Locate every blood parasite and identify its species.
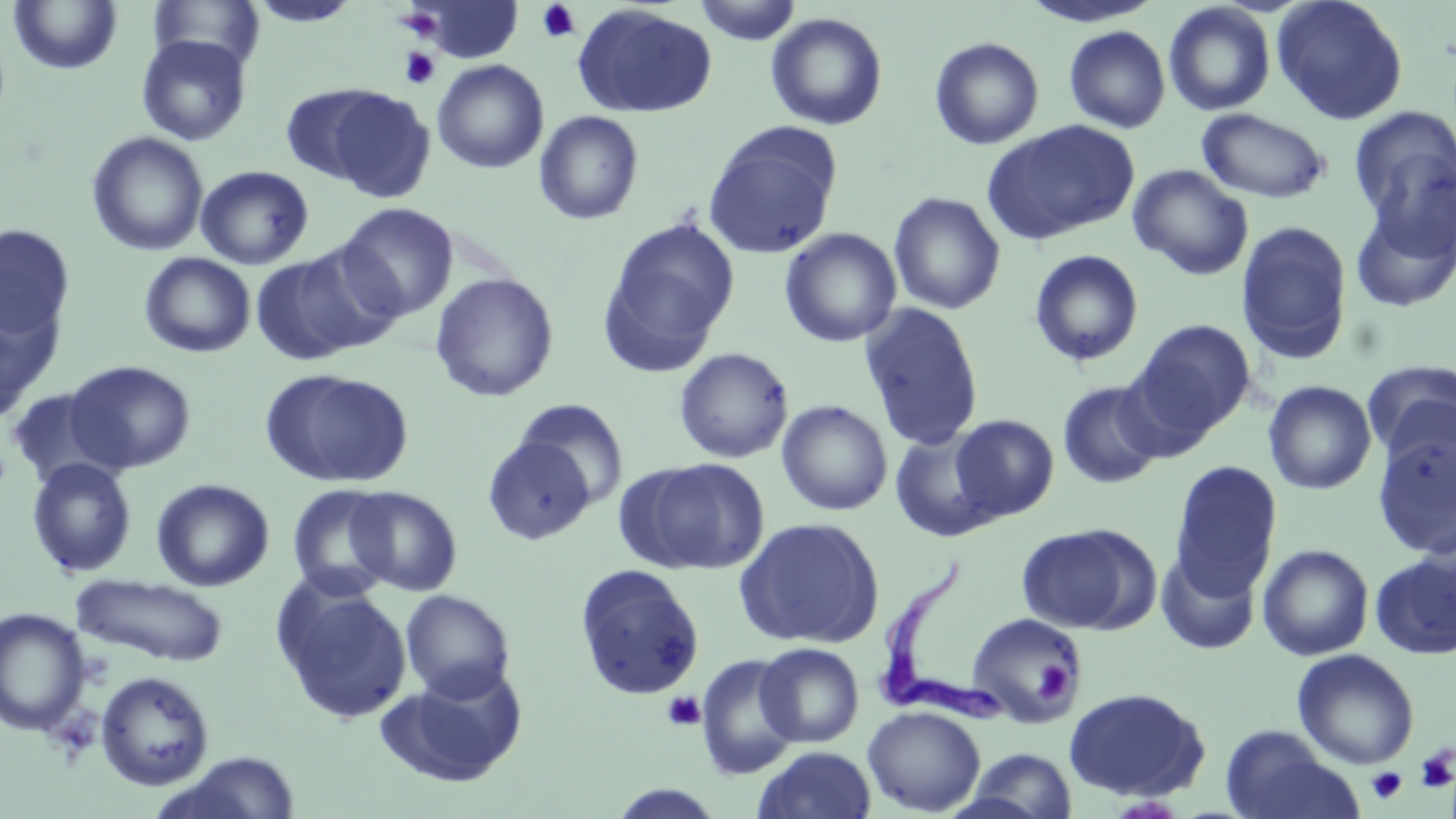
Approximate bounding boxes as named x1/y1/x2/y2 corners in pixels.
Trypanosoma brucei: (x1=876, y1=556, x2=1001, y2=721).
No Plasmodium falciparum, Plasmodium ovale, Plasmodium malariae, Plasmodium vivax, or Babesia divergens observed.

slide-level diagnosis = Trypanosoma brucei
image size = 1456×819 pixels
uninfected red blood cell locations = approximate bounding boxes as named x1/y1/x2/y2 corners in pixels: (x1=7, y1=0, x2=122, y2=76), (x1=149, y1=0, x2=265, y2=70), (x1=247, y1=0, x2=362, y2=28), (x1=692, y1=0, x2=803, y2=45), (x1=1019, y1=0, x2=1166, y2=29), (x1=1271, y1=0, x2=1409, y2=125), (x1=415, y1=1, x2=524, y2=63), (x1=1163, y1=2, x2=1276, y2=116), (x1=571, y1=5, x2=718, y2=119), (x1=399, y1=10, x2=442, y2=40), (x1=765, y1=12, x2=889, y2=131), (x1=1064, y1=26, x2=1171, y2=133), (x1=136, y1=35, x2=252, y2=146), (x1=929, y1=36, x2=1044, y2=150), (x1=432, y1=59, x2=549, y2=174), (x1=281, y1=84, x2=391, y2=186), (x1=324, y1=88, x2=437, y2=205), (x1=1349, y1=106, x2=1456, y2=240), (x1=1197, y1=108, x2=1331, y2=203), (x1=533, y1=110, x2=644, y2=226), (x1=981, y1=120, x2=1141, y2=245), (x1=702, y1=122, x2=843, y2=260), (x1=86, y1=131, x2=209, y2=256), (x1=1128, y1=164, x2=1253, y2=280), (x1=195, y1=165, x2=314, y2=269), (x1=887, y1=191, x2=1006, y2=315), (x1=1350, y1=192, x2=1456, y2=318), (x1=337, y1=202, x2=459, y2=322), (x1=598, y1=217, x2=740, y2=373), (x1=1236, y1=220, x2=1354, y2=364), (x1=0, y1=223, x2=76, y2=345), (x1=779, y1=228, x2=902, y2=348), (x1=1029, y1=249, x2=1145, y2=367), (x1=249, y1=251, x2=373, y2=366), (x1=139, y1=252, x2=256, y2=358), (x1=430, y1=272, x2=559, y2=402), (x1=0, y1=292, x2=63, y2=419), (x1=859, y1=302, x2=984, y2=451), (x1=1131, y1=319, x2=1256, y2=438), (x1=673, y1=347, x2=794, y2=464), (x1=64, y1=360, x2=196, y2=474), (x1=1361, y1=360, x2=1456, y2=463), (x1=260, y1=369, x2=414, y2=487), (x1=1057, y1=380, x2=1165, y2=489), (x1=1263, y1=380, x2=1377, y2=495), (x1=6, y1=388, x2=116, y2=489), (x1=513, y1=398, x2=629, y2=507), (x1=776, y1=399, x2=893, y2=516), (x1=771, y1=401, x2=890, y2=647), (x1=950, y1=414, x2=1059, y2=521), (x1=890, y1=431, x2=999, y2=542), (x1=1371, y1=431, x2=1456, y2=559), (x1=481, y1=434, x2=597, y2=545), (x1=26, y1=457, x2=137, y2=578), (x1=634, y1=457, x2=770, y2=574), (x1=1169, y1=460, x2=1283, y2=596), (x1=151, y1=478, x2=275, y2=591), (x1=287, y1=483, x2=399, y2=598), (x1=345, y1=486, x2=462, y2=596), (x1=734, y1=517, x2=885, y2=649), (x1=1015, y1=524, x2=1150, y2=634), (x1=1257, y1=544, x2=1374, y2=661), (x1=1156, y1=551, x2=1261, y2=655), (x1=1370, y1=552, x2=1456, y2=659), (x1=574, y1=565, x2=705, y2=701), (x1=72, y1=574, x2=229, y2=666), (x1=276, y1=582, x2=413, y2=724), (x1=400, y1=589, x2=515, y2=701), (x1=1, y1=607, x2=91, y2=735), (x1=966, y1=612, x2=1086, y2=727), (x1=755, y1=642, x2=864, y2=747), (x1=1292, y1=649, x2=1419, y2=770), (x1=695, y1=654, x2=802, y2=780), (x1=381, y1=664, x2=528, y2=787), (x1=95, y1=671, x2=215, y2=792), (x1=1062, y1=686, x2=1212, y2=802), (x1=862, y1=705, x2=985, y2=816), (x1=1220, y1=726, x2=1358, y2=819), (x1=754, y1=746, x2=877, y2=819), (x1=961, y1=748, x2=1078, y2=819), (x1=166, y1=751, x2=305, y2=818)
preparation = thin blood smear
modality = optical microscopy
stain = May-Grünwald-Giemsa
field of view = one of a larger specimen
platelet locations = approximate bounding boxes as named x1/y1/x2/y2 corners in pixels: (x1=537, y1=2, x2=581, y2=43), (x1=400, y1=47, x2=440, y2=90), (x1=1034, y1=660, x2=1076, y2=701), (x1=662, y1=691, x2=706, y2=732), (x1=1415, y1=746, x2=1456, y2=792), (x1=1366, y1=766, x2=1408, y2=804)
magnification = 1000x